State which parasite is depicted.
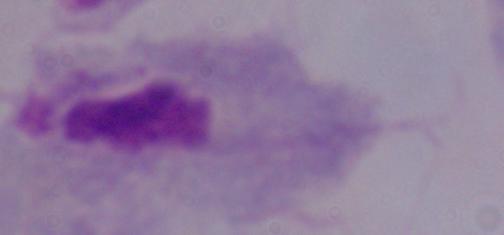

A trichomonad.

modality: photomicrograph
magnification: 1000x